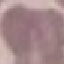 Result: no malaria parasites detected. Cell patch, automatically extracted from a larger field of view and resized to 64 × 64 pixels. Giemsa-stained preparation. Thin smear of blood. Photographed with a smartphone camera at the microscope eyepiece.